Assess this cell for malaria.
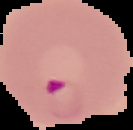

It is parasitized.

Summary:
  - Image type: segmented cell region on a black background
  - Preparation: thin blood film
  - Image size: 133×130 pixels